Classify this cell by malaria status.
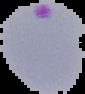

It is parasitized.

Cell region segmented out of the field of view; the surrounding area is masked to black. From a thin blood smear. Image is 85×94 pixels.